Describe the morphology of the erythrocytes.
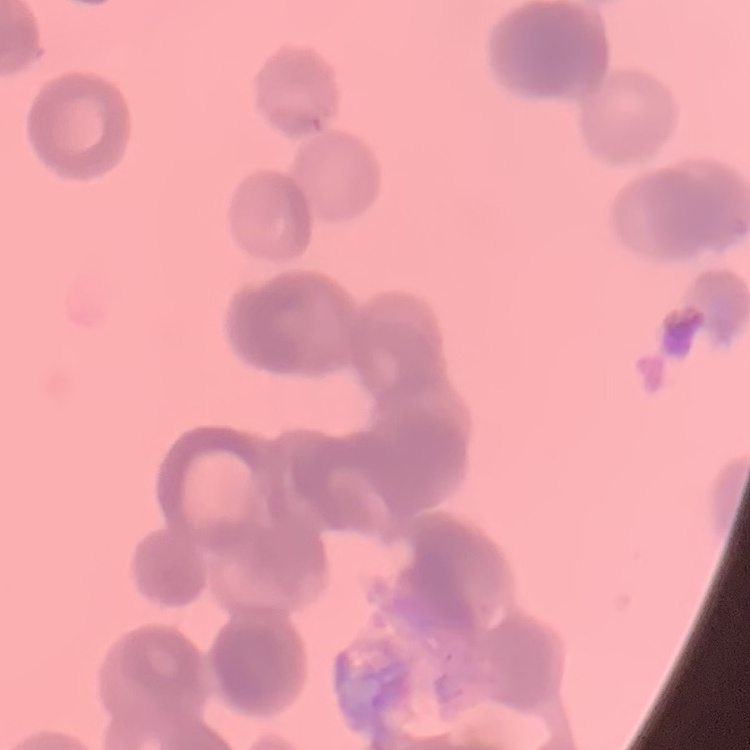

They show rouleaux formation.

Thin blood film. Square crop of a larger photomicrograph. Stained with either Field's or Giemsa.